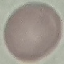
Summary:
  - Malaria status: uninfected
  - Stain: Giemsa
  - Image type: automatically extracted cell patch, resized to 64 × 64 pixels
  - Preparation: thin blood smear
  - Capture: smartphone through the microscope eyepiece